Assess this cell for malaria.
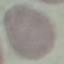

It is uninfected.

preparation = thin blood smear
stain = Giemsa
capture = smartphone camera at the microscope eyepiece
image type = cell patch, automatically extracted from a larger field of view and resized to 64 × 64 pixels